Classify this cell by malaria status.
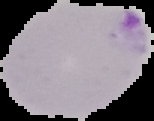

Parasitized.

preparation: thin blood film
image_type: segmented cell region on a black background
image_size: 154×121 pixels